State the blood parasite species.
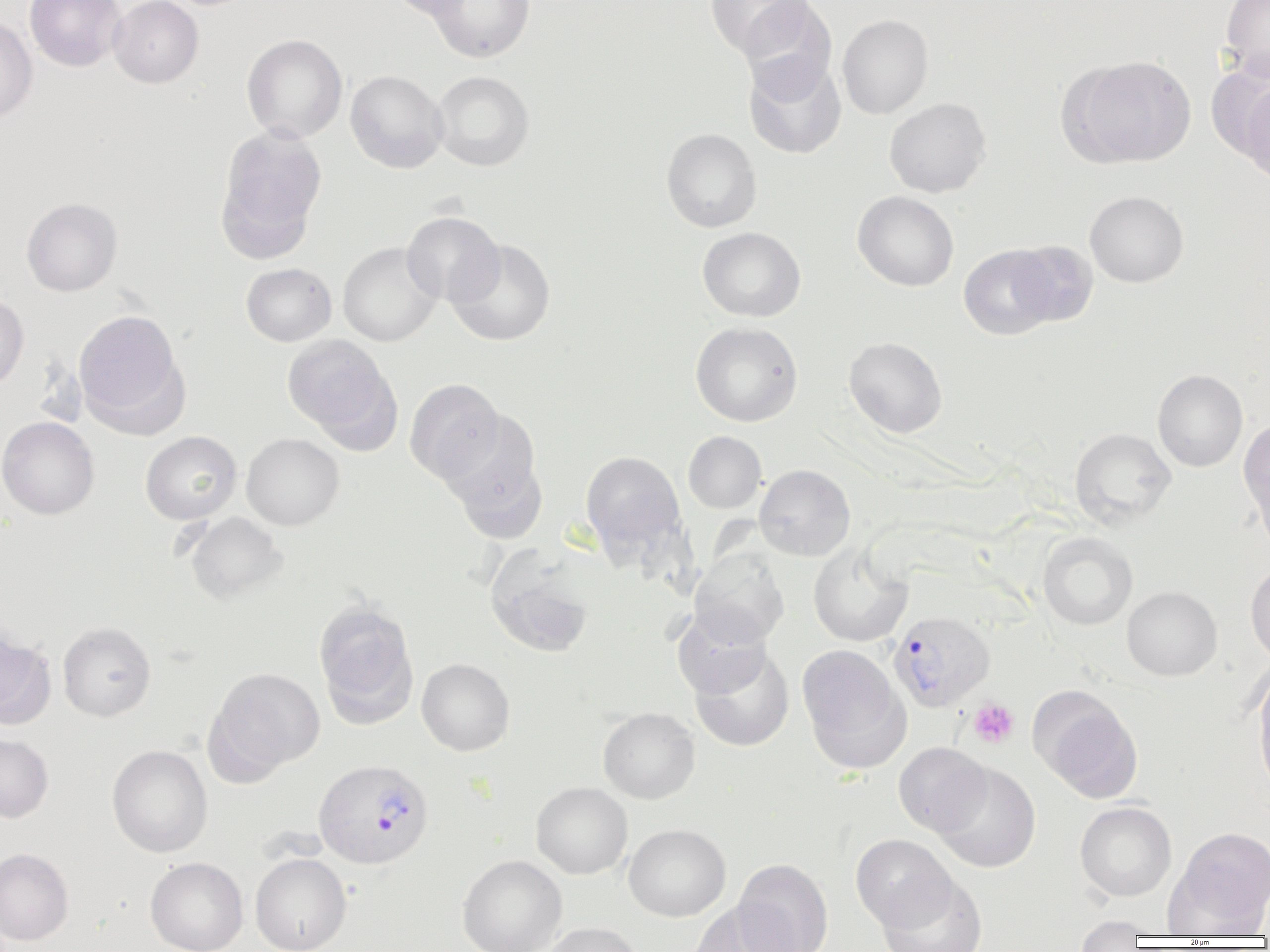

Plasmodium vivax.

modality = light microscopy
image size = 1270×952 pixels
uninfected red blood cell locations = approximate bounding boxes as named x1/y1/x2/y2 corners in pixels: (x1=24, y1=0, x2=126, y2=72), (x1=108, y1=0, x2=204, y2=88), (x1=383, y1=0, x2=477, y2=20), (x1=427, y1=0, x2=536, y2=62), (x1=1221, y1=0, x2=1270, y2=81), (x1=704, y1=1, x2=812, y2=58), (x1=738, y1=1, x2=838, y2=99), (x1=837, y1=14, x2=933, y2=119), (x1=0, y1=16, x2=38, y2=124), (x1=241, y1=34, x2=347, y2=143), (x1=743, y1=55, x2=847, y2=159), (x1=1065, y1=55, x2=1196, y2=167), (x1=345, y1=70, x2=448, y2=173), (x1=431, y1=70, x2=535, y2=171), (x1=1240, y1=77, x2=1270, y2=187), (x1=884, y1=97, x2=991, y2=198), (x1=216, y1=126, x2=327, y2=255), (x1=661, y1=128, x2=762, y2=233), (x1=852, y1=191, x2=959, y2=291), (x1=1085, y1=191, x2=1189, y2=287), (x1=21, y1=197, x2=123, y2=296), (x1=401, y1=211, x2=504, y2=306), (x1=697, y1=227, x2=806, y2=322), (x1=445, y1=238, x2=556, y2=346), (x1=1009, y1=240, x2=1098, y2=327), (x1=338, y1=242, x2=441, y2=346), (x1=958, y1=244, x2=1059, y2=340), (x1=240, y1=262, x2=337, y2=346), (x1=0, y1=293, x2=29, y2=391), (x1=73, y1=309, x2=187, y2=431), (x1=690, y1=321, x2=803, y2=427), (x1=282, y1=335, x2=399, y2=446), (x1=844, y1=336, x2=948, y2=438), (x1=1152, y1=369, x2=1248, y2=472), (x1=404, y1=378, x2=504, y2=485), (x1=439, y1=409, x2=548, y2=539), (x1=0, y1=416, x2=99, y2=520), (x1=1239, y1=417, x2=1270, y2=537), (x1=1069, y1=428, x2=1177, y2=528), (x1=140, y1=431, x2=242, y2=524), (x1=683, y1=431, x2=767, y2=513), (x1=241, y1=433, x2=344, y2=530), (x1=580, y1=451, x2=685, y2=555), (x1=754, y1=464, x2=856, y2=561), (x1=182, y1=512, x2=288, y2=604), (x1=1038, y1=532, x2=1138, y2=630), (x1=808, y1=543, x2=913, y2=646), (x1=485, y1=545, x2=597, y2=658), (x1=690, y1=550, x2=790, y2=647), (x1=1245, y1=560, x2=1270, y2=666), (x1=1122, y1=586, x2=1222, y2=681), (x1=313, y1=599, x2=418, y2=726), (x1=672, y1=609, x2=772, y2=699), (x1=57, y1=621, x2=156, y2=721), (x1=0, y1=628, x2=56, y2=730), (x1=797, y1=644, x2=910, y2=771), (x1=689, y1=646, x2=795, y2=751), (x1=416, y1=658, x2=515, y2=756), (x1=1252, y1=664, x2=1270, y2=796), (x1=206, y1=667, x2=325, y2=778), (x1=1031, y1=688, x2=1144, y2=802), (x1=598, y1=707, x2=700, y2=803), (x1=0, y1=732, x2=53, y2=823), (x1=893, y1=742, x2=992, y2=836), (x1=107, y1=745, x2=213, y2=857), (x1=933, y1=762, x2=1041, y2=873), (x1=531, y1=782, x2=633, y2=879), (x1=1075, y1=801, x2=1177, y2=901), (x1=624, y1=824, x2=731, y2=921), (x1=1168, y1=826, x2=1270, y2=934), (x1=850, y1=834, x2=956, y2=930), (x1=0, y1=847, x2=74, y2=945), (x1=250, y1=853, x2=351, y2=952), (x1=456, y1=854, x2=567, y2=952), (x1=145, y1=857, x2=248, y2=952), (x1=733, y1=858, x2=834, y2=952), (x1=876, y1=873, x2=987, y2=952), (x1=687, y1=901, x2=798, y2=952), (x1=1072, y1=916, x2=1150, y2=950), (x1=538, y1=921, x2=644, y2=952)
field of view = single
Plasmodium vivax-infected red blood cell locations = approximate bounding boxes as named x1/y1/x2/y2 corners in pixels: (x1=889, y1=611, x2=996, y2=712), (x1=313, y1=758, x2=434, y2=870)
magnification = 1000x
platelet locations = approximate bounding boxes as named x1/y1/x2/y2 corners in pixels: (x1=968, y1=699, x2=1019, y2=748)
preparation = thin blood film